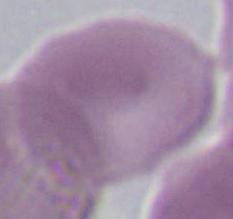
Photomicrograph. A red blood cell is seen. 1000x magnification.